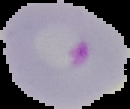
From a thin blood smear. Malaria status: parasitized. Image is 130×109 pixels. The area outside the segmented cell region is set to black.